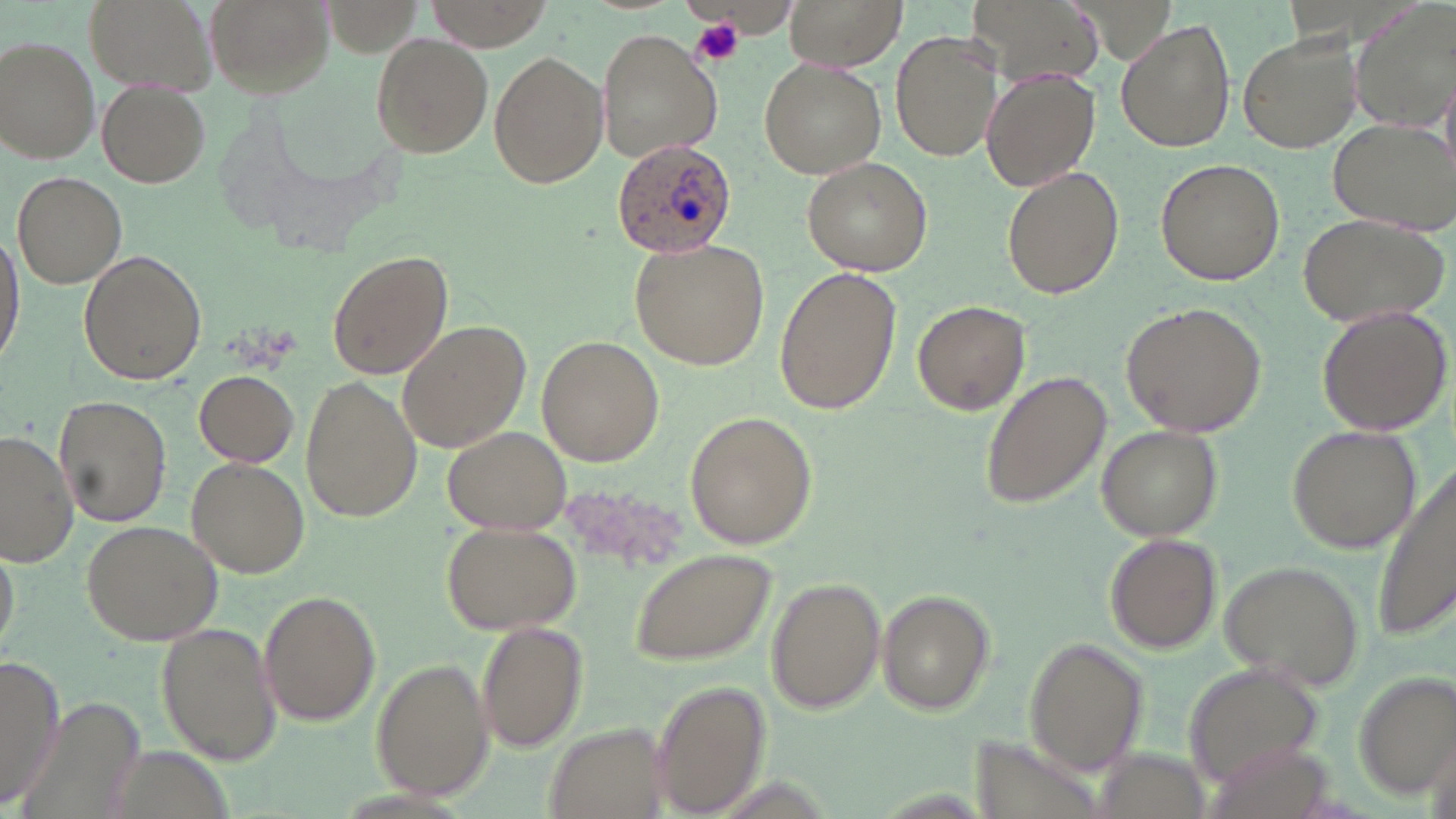

Approximate bounding boxes as named x1/y1/x2/y2 corners in pixels. Uninfected red blood cell locations: (x1=85, y1=0, x2=219, y2=101), (x1=201, y1=0, x2=333, y2=99), (x1=422, y1=0, x2=554, y2=52), (x1=786, y1=0, x2=907, y2=70), (x1=965, y1=0, x2=1101, y2=89), (x1=1350, y1=2, x2=1455, y2=133), (x1=1116, y1=21, x2=1236, y2=153), (x1=891, y1=28, x2=1004, y2=161), (x1=598, y1=29, x2=722, y2=162), (x1=1237, y1=31, x2=1363, y2=153), (x1=371, y1=32, x2=492, y2=157), (x1=0, y1=35, x2=100, y2=163), (x1=488, y1=50, x2=608, y2=188), (x1=759, y1=58, x2=887, y2=178), (x1=981, y1=68, x2=1101, y2=191), (x1=1440, y1=73, x2=1456, y2=181), (x1=96, y1=81, x2=211, y2=189), (x1=1328, y1=118, x2=1456, y2=233), (x1=802, y1=157, x2=932, y2=277), (x1=1154, y1=158, x2=1285, y2=286), (x1=1001, y1=167, x2=1124, y2=300), (x1=12, y1=172, x2=126, y2=289), (x1=1296, y1=211, x2=1449, y2=327), (x1=0, y1=234, x2=24, y2=369), (x1=631, y1=237, x2=771, y2=370), (x1=326, y1=248, x2=454, y2=381), (x1=79, y1=250, x2=206, y2=386), (x1=775, y1=268, x2=901, y2=414), (x1=912, y1=299, x2=1031, y2=417), (x1=1121, y1=301, x2=1267, y2=436), (x1=1315, y1=305, x2=1452, y2=437), (x1=396, y1=320, x2=530, y2=452), (x1=537, y1=334, x2=663, y2=468), (x1=194, y1=370, x2=298, y2=466), (x1=982, y1=372, x2=1112, y2=508), (x1=301, y1=376, x2=422, y2=519), (x1=56, y1=395, x2=173, y2=527), (x1=684, y1=410, x2=817, y2=549), (x1=441, y1=423, x2=571, y2=537), (x1=1096, y1=425, x2=1223, y2=541), (x1=1287, y1=425, x2=1421, y2=553), (x1=0, y1=430, x2=78, y2=566), (x1=186, y1=456, x2=311, y2=577), (x1=1370, y1=457, x2=1456, y2=640), (x1=82, y1=517, x2=224, y2=645), (x1=441, y1=521, x2=582, y2=636), (x1=1105, y1=533, x2=1223, y2=654), (x1=0, y1=536, x2=23, y2=659), (x1=629, y1=548, x2=777, y2=666), (x1=1217, y1=557, x2=1364, y2=692), (x1=768, y1=576, x2=886, y2=713), (x1=876, y1=589, x2=993, y2=714), (x1=259, y1=590, x2=382, y2=726), (x1=479, y1=620, x2=588, y2=753), (x1=156, y1=622, x2=282, y2=765), (x1=1024, y1=635, x2=1149, y2=775), (x1=0, y1=658, x2=63, y2=808), (x1=372, y1=659, x2=492, y2=799), (x1=1182, y1=660, x2=1325, y2=792), (x1=1354, y1=670, x2=1454, y2=800), (x1=650, y1=681, x2=773, y2=816). Plasmodium ovale-infected red blood cell locations: (x1=611, y1=138, x2=738, y2=258). Platelet locations: (x1=690, y1=17, x2=745, y2=69). Slide-level diagnosis: Plasmodium ovale. Thin blood smear. 1000x magnification. Single field of view. Optical microscopy. Image is 1456×819 pixels. May-Grünwald-Giemsa stain.